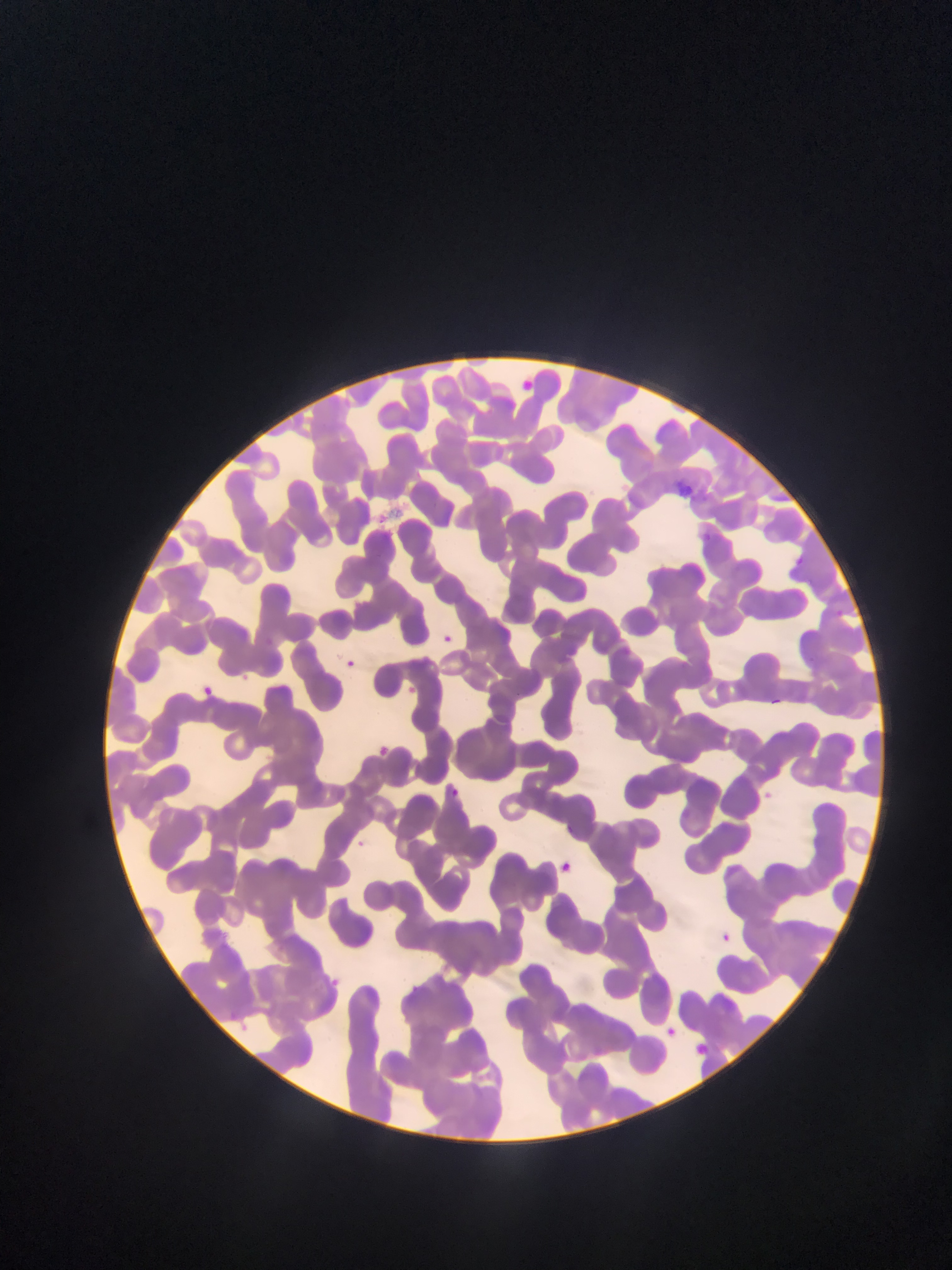
Approximate bounding boxes as left top right bottom in pixels.
Summary:
  - Malaria parasite locations: 444 632 454 649; 347 659 353 670; 202 683 223 699; 403 686 422 695; 768 697 788 711; 378 737 392 755; 450 787 459 794; 766 789 778 807; 556 859 575 873; 722 932 736 942; 328 974 343 993; 658 1017 682 1037; 697 1041 708 1055 | approximate x y pixel centers of objects too small to bound: 359 843
  - Image size: 952×1270 pixels
  - Preparation: thin blood smear
  - Field of view: single
  - Capture: mobile-phone photograph through a microscope
  - Country: Ghana